Report the malaria status of this cell.
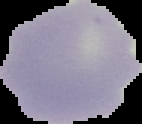

Uninfected.

image type = cell region segmented out of the field of view; surrounding area masked to black
image size = 142×124 pixels
preparation = thin blood film